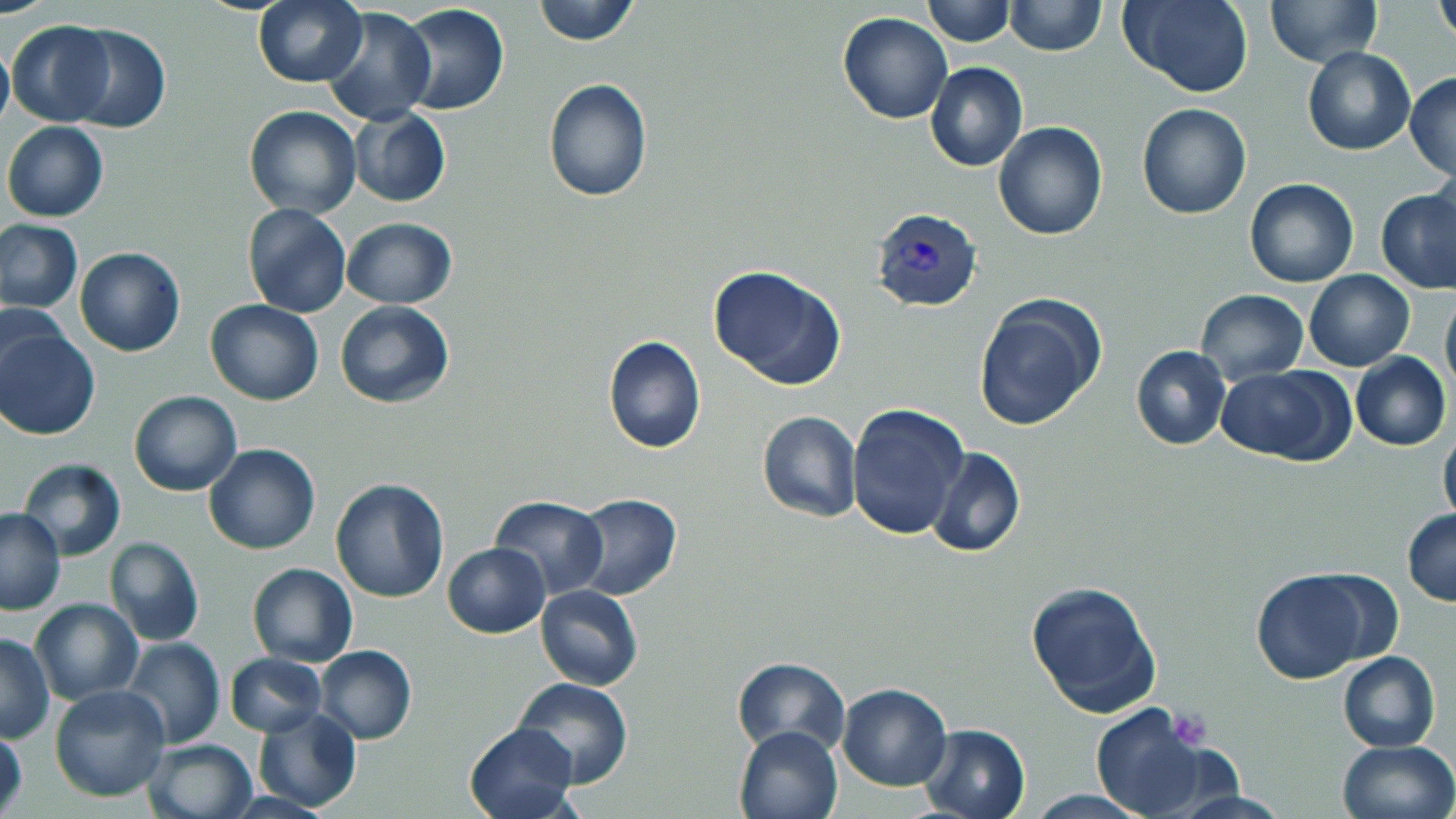

Summary:
  - Coordinate format: approximate bounding boxes as named x1/y1/x2/y2 corners in pixels
  - Plasmodium vivax-infected red blood cell locations: (x1=871, y1=206, x2=983, y2=312)
  - Platelet locations: (x1=1173, y1=709, x2=1210, y2=751)
  - Uninfected red blood cell locations: (x1=533, y1=0, x2=639, y2=45), (x1=921, y1=0, x2=1014, y2=47), (x1=1122, y1=0, x2=1255, y2=98), (x1=1263, y1=0, x2=1381, y2=67), (x1=253, y1=1, x2=367, y2=88), (x1=1004, y1=1, x2=1106, y2=57), (x1=397, y1=3, x2=510, y2=116), (x1=1434, y1=4, x2=1456, y2=47), (x1=323, y1=10, x2=434, y2=125), (x1=838, y1=12, x2=953, y2=125), (x1=6, y1=19, x2=116, y2=126), (x1=64, y1=25, x2=169, y2=133), (x1=0, y1=36, x2=13, y2=138), (x1=1302, y1=47, x2=1415, y2=155), (x1=924, y1=61, x2=1027, y2=173), (x1=1405, y1=72, x2=1456, y2=181), (x1=542, y1=79, x2=653, y2=203), (x1=1137, y1=102, x2=1253, y2=219), (x1=243, y1=105, x2=362, y2=219), (x1=348, y1=106, x2=451, y2=207), (x1=2, y1=121, x2=108, y2=223), (x1=994, y1=121, x2=1107, y2=241), (x1=1245, y1=178, x2=1359, y2=287), (x1=1377, y1=187, x2=1455, y2=294), (x1=244, y1=203, x2=351, y2=318), (x1=340, y1=217, x2=458, y2=307), (x1=0, y1=220, x2=82, y2=314), (x1=74, y1=247, x2=185, y2=356), (x1=708, y1=265, x2=846, y2=390), (x1=1304, y1=270, x2=1415, y2=370), (x1=1195, y1=290, x2=1310, y2=383), (x1=1441, y1=292, x2=1456, y2=400), (x1=974, y1=295, x2=1105, y2=432), (x1=205, y1=299, x2=323, y2=405), (x1=334, y1=300, x2=454, y2=408), (x1=1, y1=302, x2=72, y2=401), (x1=0, y1=327, x2=100, y2=441), (x1=602, y1=334, x2=705, y2=453), (x1=1129, y1=345, x2=1232, y2=450), (x1=1350, y1=352, x2=1452, y2=450), (x1=1216, y1=365, x2=1354, y2=466), (x1=128, y1=391, x2=242, y2=496), (x1=845, y1=403, x2=968, y2=543), (x1=756, y1=412, x2=860, y2=523), (x1=1438, y1=422, x2=1456, y2=530), (x1=204, y1=444, x2=320, y2=554), (x1=925, y1=447, x2=1024, y2=559), (x1=19, y1=458, x2=126, y2=560), (x1=330, y1=478, x2=451, y2=603), (x1=571, y1=493, x2=682, y2=599), (x1=489, y1=496, x2=609, y2=600), (x1=0, y1=507, x2=65, y2=616), (x1=1402, y1=509, x2=1456, y2=605), (x1=104, y1=537, x2=204, y2=647), (x1=441, y1=542, x2=549, y2=637), (x1=247, y1=564, x2=358, y2=666), (x1=1248, y1=567, x2=1390, y2=684), (x1=1026, y1=579, x2=1162, y2=718), (x1=535, y1=584, x2=643, y2=691), (x1=29, y1=598, x2=141, y2=704), (x1=1, y1=633, x2=53, y2=742), (x1=119, y1=638, x2=226, y2=749), (x1=315, y1=645, x2=417, y2=745), (x1=1338, y1=650, x2=1440, y2=751), (x1=225, y1=652, x2=328, y2=737), (x1=730, y1=656, x2=850, y2=758), (x1=514, y1=677, x2=633, y2=789), (x1=835, y1=683, x2=951, y2=792), (x1=49, y1=685, x2=171, y2=802), (x1=1089, y1=703, x2=1220, y2=817), (x1=252, y1=706, x2=362, y2=813), (x1=462, y1=721, x2=582, y2=819), (x1=733, y1=723, x2=842, y2=819), (x1=918, y1=723, x2=1031, y2=819), (x1=0, y1=725, x2=27, y2=819), (x1=143, y1=738, x2=257, y2=819), (x1=1336, y1=739, x2=1455, y2=819), (x1=1022, y1=789, x2=1159, y2=818), (x1=1163, y1=789, x2=1299, y2=818)
  - Slide-level diagnosis: Plasmodium vivax
  - Preparation: thin blood smear
  - Field of view: single
  - Magnification: 1000x
  - Modality: light microscopy
  - Stain: May-Grünwald-Giemsa
  - Image size: 1456×819 pixels